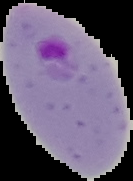

Segmented cell region on a black background. From a thin blood smear. Result: Plasmodium parasites identified. Image is 133×181 pixels.